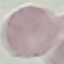
Summary:
  - Result: no malaria parasites detected
  - Image type: automatically extracted cell patch, resized to 64 × 64 pixels
  - Capture: smartphone camera at the microscope eyepiece
  - Preparation: thin blood film
  - Stain: Giemsa